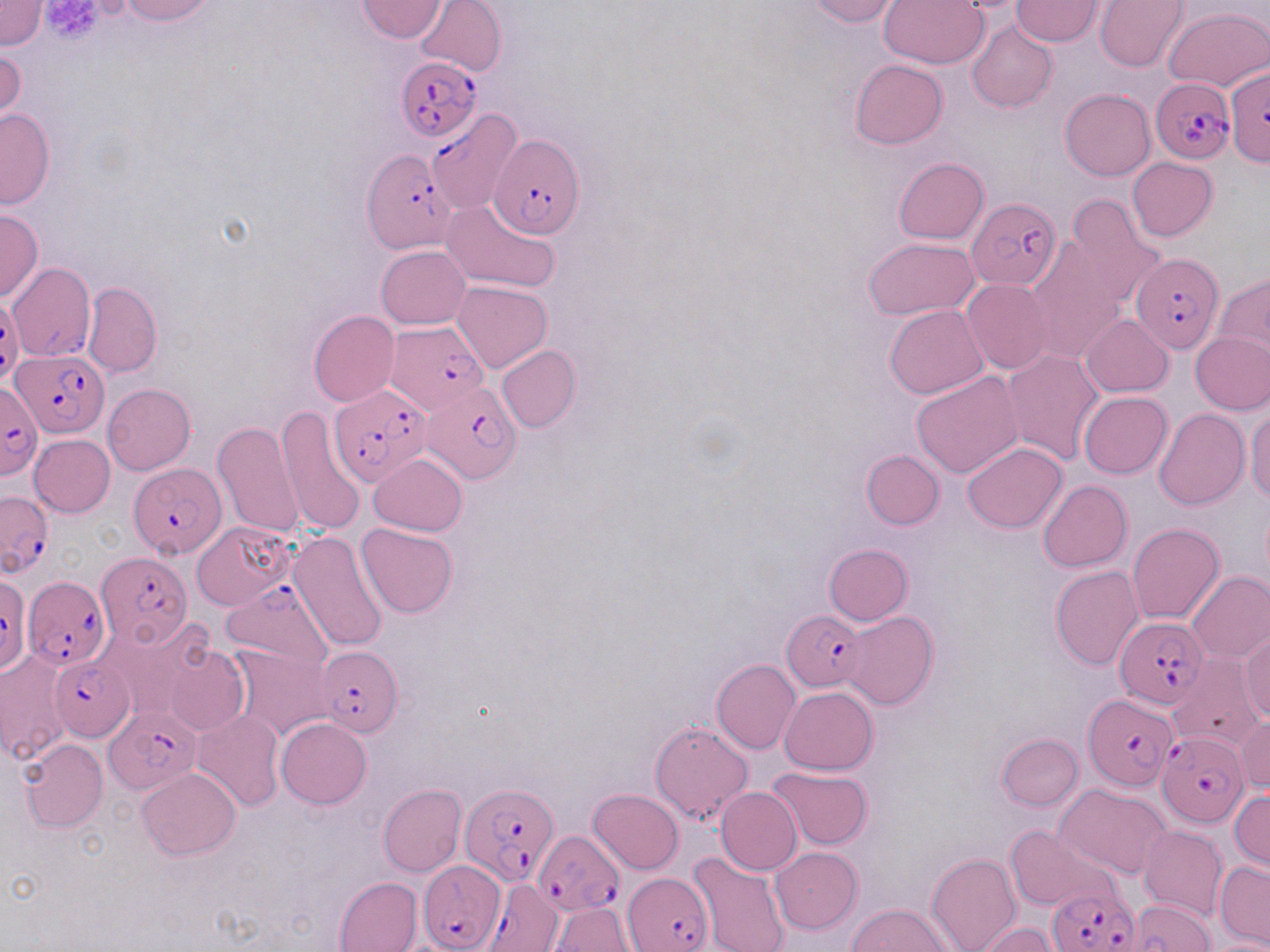

slide-level diagnosis = Plasmodium falciparum
image size = 1270×952 pixels
stain = May-Grünwald-Giemsa
Plasmodium falciparum-infected red blood cell locations = approximate bounding boxes as (x1,y1)-(x2,y2) corner pairs in pixels: (397,56)-(482,144), (1230,62)-(1270,179), (1150,77)-(1234,163), (427,109)-(523,213), (488,133)-(584,239), (362,150)-(457,254), (967,198)-(1059,289), (1133,252)-(1224,353), (8,263)-(95,362), (0,298)-(21,385), (385,323)-(488,415), (12,349)-(107,437), (420,375)-(522,481), (0,383)-(42,479), (329,383)-(432,488), (128,463)-(228,558), (1,490)-(53,575), (94,552)-(191,647), (1,575)-(30,675), (24,577)-(110,670), (222,580)-(336,669), (782,611)-(864,691), (1115,616)-(1208,707), (314,647)-(401,736), (48,656)-(135,739), (1083,694)-(1177,791), (103,706)-(201,794), (1157,732)-(1247,827), (462,781)-(557,885), (533,830)-(624,916), (418,861)-(506,951), (622,872)-(712,952), (484,878)-(562,952), (1047,888)-(1138,952)
modality = light microscopy
platelet locations = approximate bounding boxes as (x1,y1)-(x2,y2) corner pairs in pixels: (39,0)-(104,42)
magnification = 1000x
uninfected red blood cell locations = approximate bounding boxes as (x1,y1)-(x2,y2) corner pairs in pixels: (0,0)-(46,49), (117,0)-(215,24), (414,0)-(506,75), (803,0)-(900,26), (356,1)-(450,42), (880,1)-(989,69), (1010,1)-(1105,46), (1094,1)-(1189,72), (1163,6)-(1270,92), (967,21)-(1058,114), (0,43)-(25,128), (851,59)-(948,148), (1060,88)-(1155,181), (0,108)-(54,209), (893,157)-(989,244), (1127,157)-(1217,241), (1065,194)-(1168,309), (441,199)-(561,293), (0,208)-(44,303), (863,238)-(980,321), (1025,240)-(1125,360), (377,245)-(470,328), (1014,253)-(1113,449), (1213,273)-(1270,363), (962,278)-(1053,374), (83,281)-(162,377), (452,281)-(551,372), (885,304)-(989,399), (308,309)-(399,407), (1080,313)-(1174,396), (1190,332)-(1270,414), (497,344)-(580,433), (1002,348)-(1104,465), (911,371)-(1024,478), (102,383)-(195,475), (1067,389)-(1163,553), (1078,391)-(1172,479), (274,403)-(368,536), (1154,407)-(1250,509), (1245,407)-(1269,503), (213,423)-(305,538), (29,435)-(115,517), (961,442)-(1067,534), (861,449)-(944,530), (368,455)-(467,536), (1039,480)-(1131,572), (192,520)-(294,610), (356,522)-(457,618), (1126,522)-(1225,625), (288,529)-(390,654), (824,544)-(912,625), (1050,566)-(1144,670), (1186,570)-(1270,662), (845,612)-(938,711), (96,617)-(212,720), (1239,631)-(1270,723), (228,644)-(333,740), (163,645)-(249,737), (0,651)-(71,766), (1168,653)-(1264,754), (711,659)-(800,754), (781,686)-(878,774), (191,709)-(283,812), (1233,716)-(1270,794), (276,717)-(371,809), (649,720)-(754,824), (996,733)-(1083,810), (19,739)-(108,832), (766,766)-(873,849), (136,768)-(240,860), (377,784)-(465,876), (1056,784)-(1173,879), (715,786)-(802,875), (589,788)-(684,874), (1230,790)-(1269,872), (1005,824)-(1111,912), (1137,825)-(1227,921), (772,847)-(862,933), (687,851)-(791,952), (927,852)-(1021,952), (1215,861)-(1270,949), (332,876)-(422,952), (1127,898)-(1218,952), (847,903)-(953,952), (550,904)-(637,950), (980,921)-(1060,952), (1209,940)-(1270,952)
field of view = one of a larger specimen
preparation = thin blood smear